State which parasite is depicted.
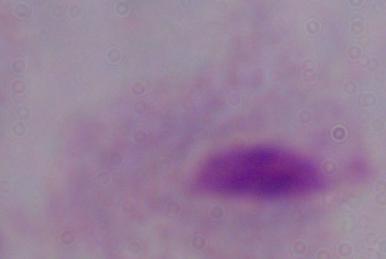

A trichomonad.

Photomicrograph. 1000x magnification.